State which parasite is depicted.
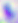

This is Toxoplasma gondii.

400x magnification. Photomicrograph.